Name the parasite shown.
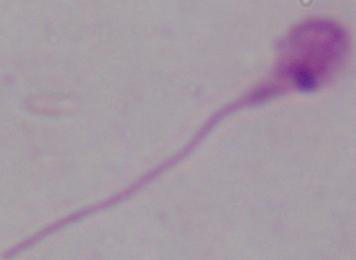

Leishmania.

1000x magnification. Micrograph.